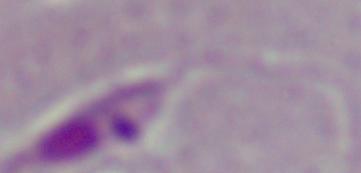
Micrograph. 1000x magnification. A Leishmania parasite is seen.